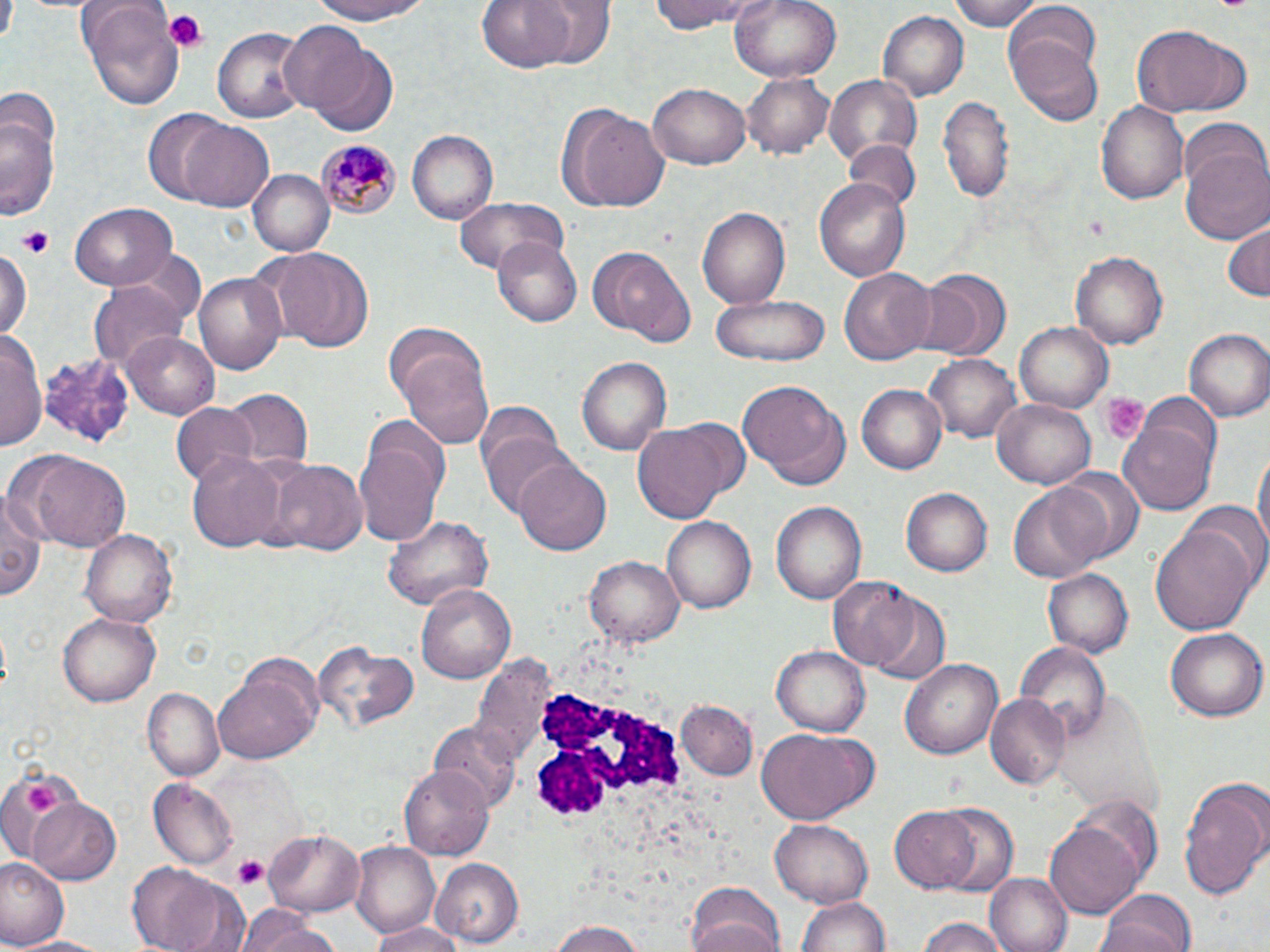
Summary:
  - Coordinate format: approximate bounding boxes as (x1,y1)-(x2,y2) corner pairs in pixels
  - Plasmodium malariae-infected red blood cell locations: (315,139)-(401,220)
  - White blood cell locations: (531,685)-(690,822)
  - Platelet locations: (163,9)-(206,50), (18,224)-(55,259), (1099,394)-(1148,443), (24,781)-(62,819), (233,857)-(268,890)
  - Uninfected red blood cell locations: (76,0)-(185,110), (306,0)-(436,24), (478,0)-(580,74), (535,0)-(618,71), (647,0)-(765,33), (729,0)-(842,84), (947,0)-(1046,30), (1005,5)-(1103,79), (879,11)-(967,101), (278,21)-(378,118), (212,25)-(309,125), (1130,25)-(1244,114), (1008,35)-(1103,127), (307,45)-(399,138), (740,69)-(834,159), (828,75)-(921,169), (647,82)-(752,169), (1,88)-(61,159), (935,96)-(1014,204), (1096,98)-(1191,206), (558,103)-(669,214), (141,109)-(230,204), (0,116)-(59,220), (180,120)-(276,212), (406,131)-(496,224), (845,140)-(920,214), (1181,147)-(1270,245), (249,169)-(334,257), (814,178)-(911,285), (454,196)-(569,274), (69,202)-(178,291), (697,208)-(790,306), (1221,221)-(1269,303), (492,236)-(582,326), (0,244)-(30,346), (591,246)-(692,345), (271,248)-(376,354), (1070,251)-(1168,350), (837,266)-(935,367), (916,268)-(1010,360), (195,272)-(287,376), (88,282)-(186,369), (710,296)-(830,365), (1015,320)-(1115,414), (1,327)-(45,456), (124,329)-(219,417), (1185,329)-(1269,423), (393,337)-(493,448), (926,351)-(1022,441), (40,353)-(138,453), (578,355)-(671,457), (736,380)-(850,488), (856,385)-(946,474), (221,390)-(310,472), (1139,392)-(1222,477), (990,398)-(1097,489), (169,402)-(260,490), (471,402)-(561,484), (355,418)-(450,546), (1119,421)-(1217,515), (630,423)-(727,526), (482,435)-(580,521), (1252,442)-(1268,565), (16,449)-(133,552), (185,450)-(289,554), (514,457)-(612,553), (272,459)-(368,556), (1056,467)-(1145,565), (1007,481)-(1111,586), (902,487)-(992,577), (1,488)-(45,606), (1184,499)-(1270,595), (770,500)-(865,607), (385,513)-(491,613), (660,517)-(754,615), (1150,521)-(1258,638), (82,527)-(177,629), (582,553)-(684,649), (1042,569)-(1134,659), (830,578)-(925,677), (418,580)-(517,684), (870,597)-(950,687), (58,611)-(161,707), (1165,628)-(1265,721), (1015,644)-(1110,741), (315,645)-(417,735), (772,645)-(870,736), (901,658)-(1004,759), (214,663)-(319,763), (141,689)-(224,782), (985,694)-(1069,789), (679,702)-(756,780), (429,721)-(520,818), (756,729)-(874,826), (0,763)-(84,863), (398,764)-(494,860), (1179,774)-(1270,898), (150,778)-(238,869), (28,798)-(123,884), (932,804)-(1020,897), (890,805)-(984,893), (771,818)-(873,908), (1045,823)-(1142,919), (263,829)-(365,914), (349,843)-(442,933), (0,857)-(67,946), (433,859)-(524,948), (124,862)-(246,952), (985,873)-(1072,952), (685,884)-(787,952), (1093,888)-(1200,952), (798,895)-(890,952), (234,910)-(345,952), (915,916)-(1011,952), (365,922)-(471,952), (543,923)-(651,952), (11,935)-(115,952)
  - Slide-level diagnosis: Plasmodium malariae
  - Preparation: thin blood film
  - Stain: May-Grünwald-Giemsa
  - Image size: 1270×952 pixels
  - Modality: optical microscopy
  - Magnification: 1000x
  - Field of view: one of a larger specimen